Report the malaria status of this cell.
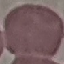

It is uninfected.

{
  "preparation": "thin blood smear",
  "stain": "Giemsa",
  "image_type": "automatically extracted cell patch, resized to 64 × 64 pixels",
  "capture": "smartphone through the microscope eyepiece"
}